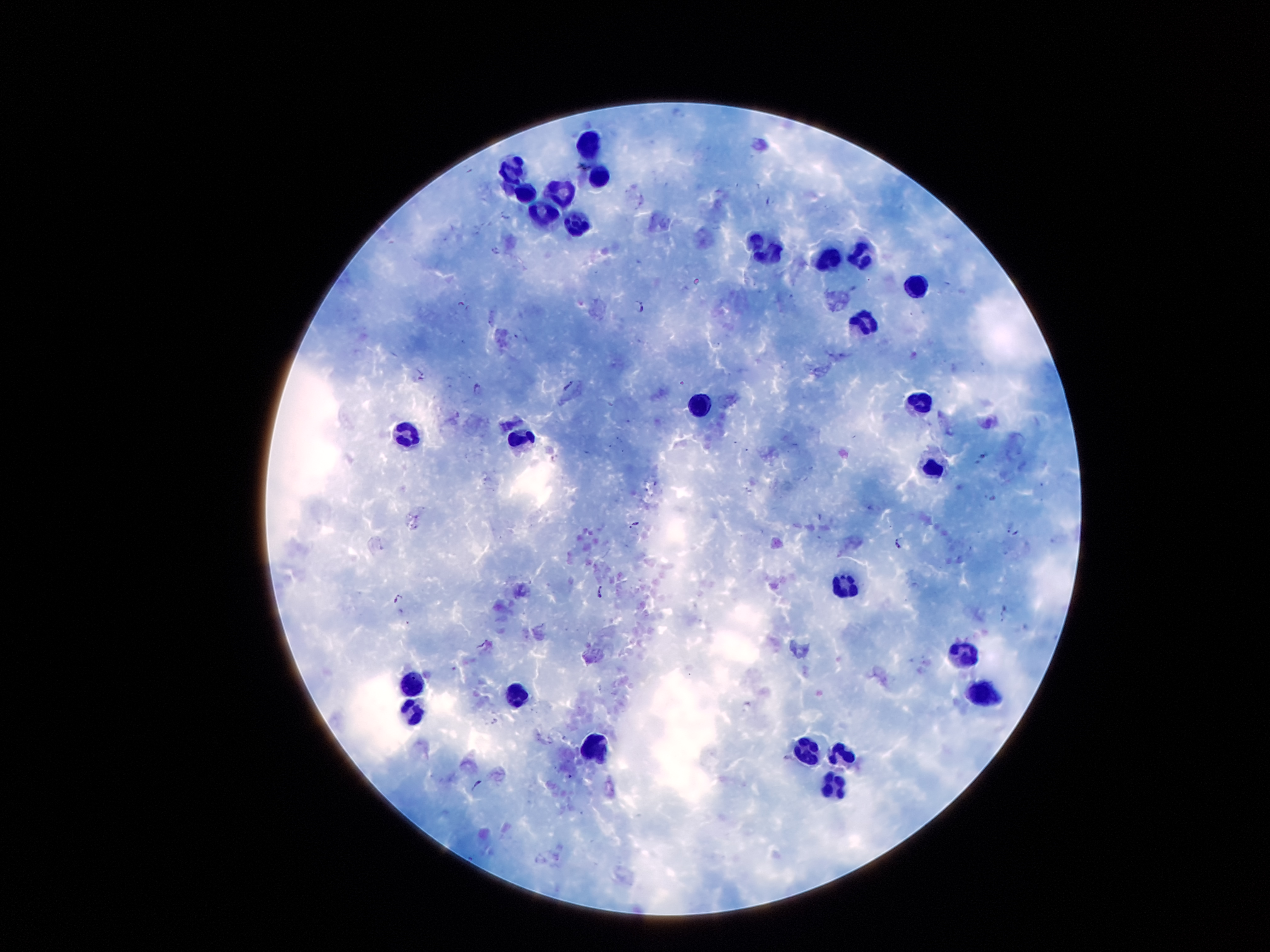
Approximate centers as {x, y} in pixels. Malaria parasite locations: {768, 199}, {643, 200}, {504, 215}, {496, 250}, {462, 304}, {638, 306}, {422, 377}, {479, 387}, {635, 524}, {1014, 532}, {900, 543}, {602, 594}, {399, 597}, {1004, 613}, {477, 785}. Leukocyte locations: {588, 144}, {517, 171}, {598, 180}, {529, 196}, {561, 196}, {545, 215}, {573, 225}, {768, 251}, {861, 255}, {826, 262}, {911, 288}, {862, 324}, {919, 401}, {694, 406}, {412, 432}, {520, 443}, {932, 468}, {844, 583}, {965, 656}, {417, 685}, {982, 694}, {516, 698}, {414, 706}, {593, 747}, {844, 751}, {813, 755}, {832, 786}. Patient malaria status: infected with Plasmodium falciparum. Single field of view. Giemsa-stained preparation. 100x magnification. Image is 1270×952 pixels. Thick peripheral-blood smear. Photographed through the microscope eyepiece with a smartphone camera.